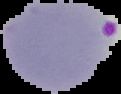
Cell region segmented out of the field of view; the surrounding area is masked to black. From a thin blood smear. Malaria status: parasitized. Image is 121×94 pixels.